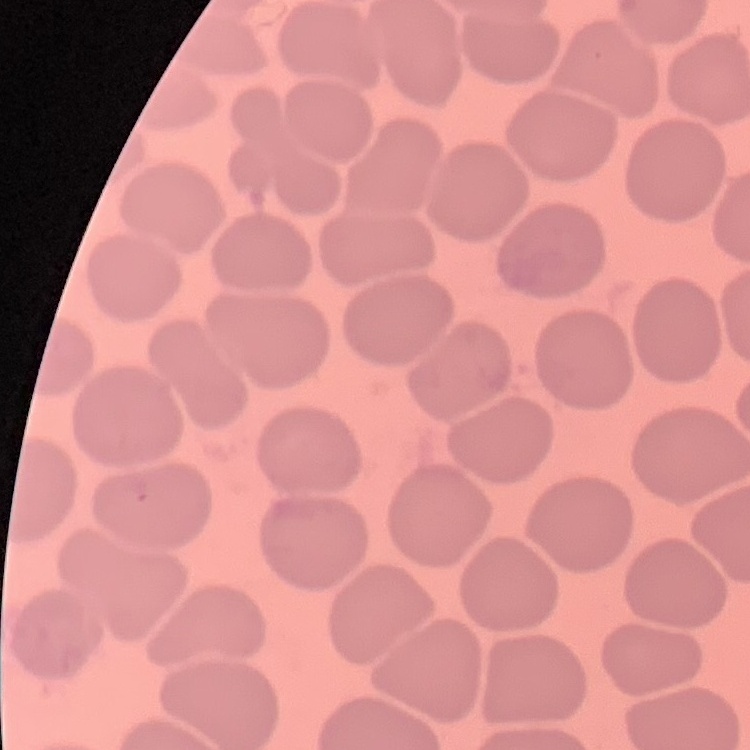 The red blood cells exhibit no rouleaux formation. Stained with either Field's or Giemsa. Square crop of a larger photomicrograph. Thin peripheral smear.